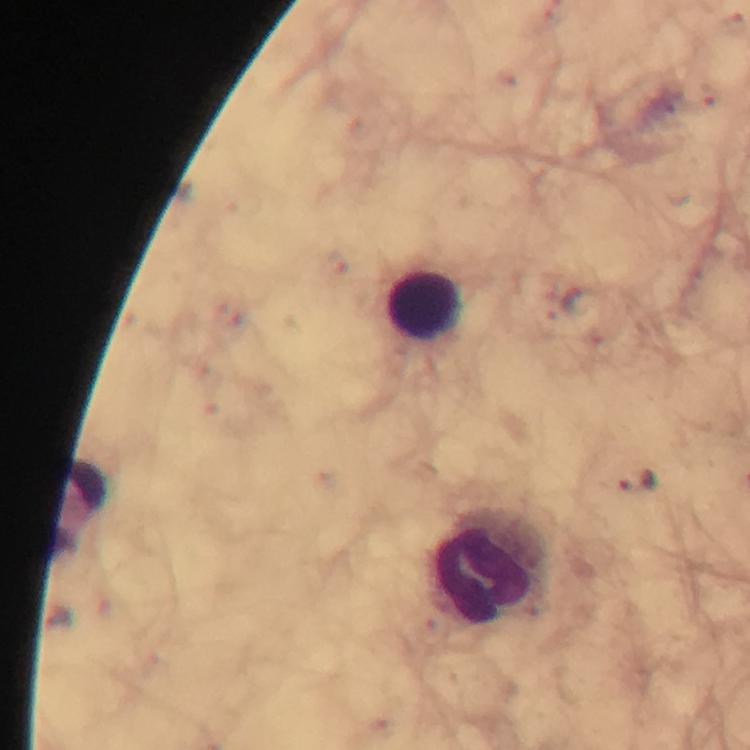
{
  "stain": "Giemsa",
  "preparation": "thick smear",
  "immersion_oil": "applied",
  "image_size": "750×750 pixels",
  "magnification": "100x",
  "cropped_from": "one field of view",
  "context": "from a malaria diagnostic workup",
  "capture": "smartphone camera through the microscope",
  "leukocyte_locations": "approximate object centers, in pixels from the top-left corner: (x=424, y=305), (x=77, y=509), (x=490, y=567)",
  "malaria_parasite_locations": "approximate object centers, in pixels from the top-left corner: (x=637, y=480)"
}